State the preparation type.
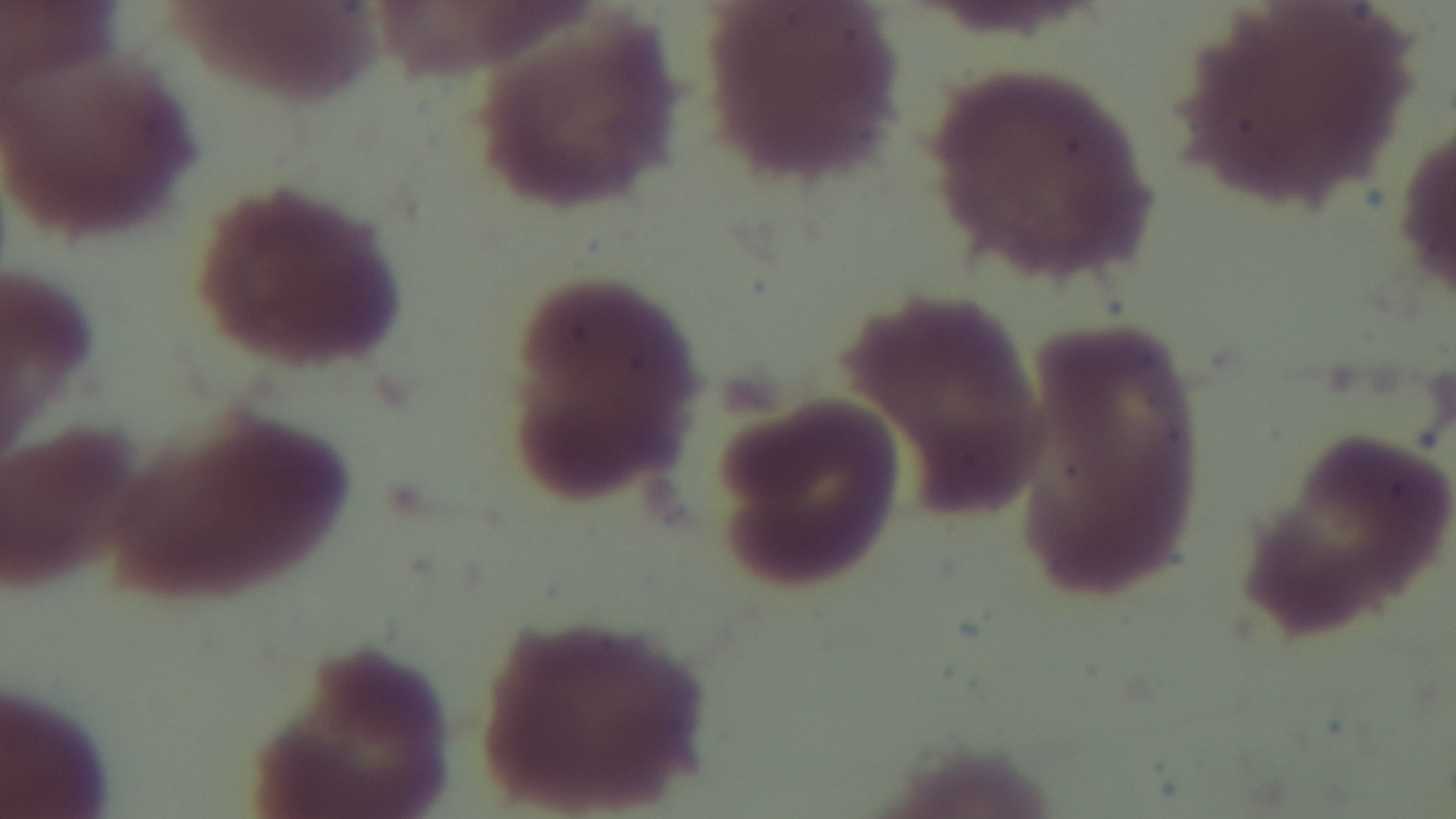
It is a thin blood film.

malaria status = uninfected
modality = light microscopy
field of view = single
capture = mounted 4K digital camera
objective = 100x oil immersion
stain = Giemsa